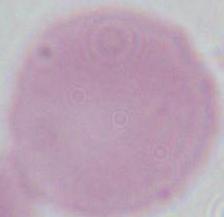
An erythrocyte is seen. Captured at 1000x magnification. Micrograph.